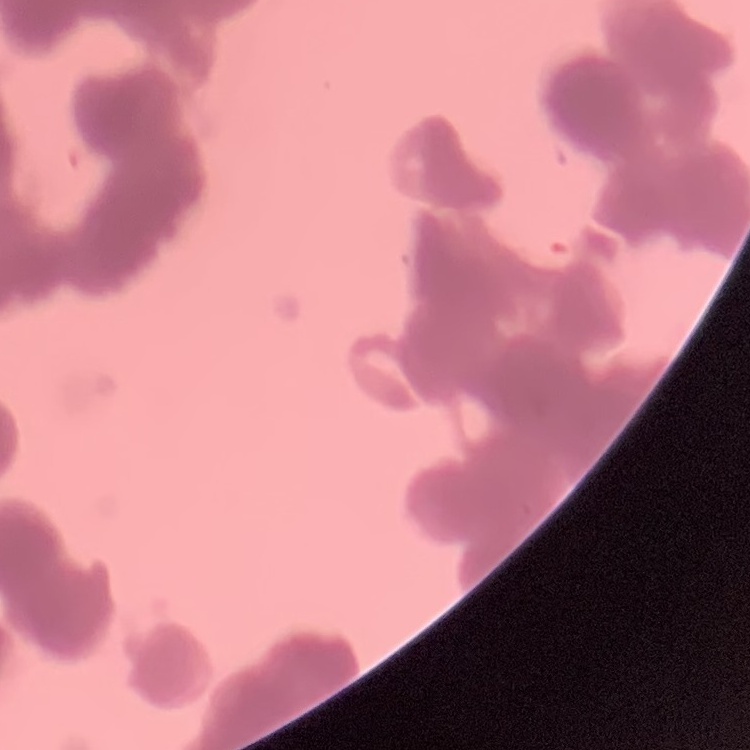
The red blood cells show rouleaux formation. Thin blood smear. Stained with either Field's or Giemsa. Square crop of a larger photomicrograph.